Report the malaria status.
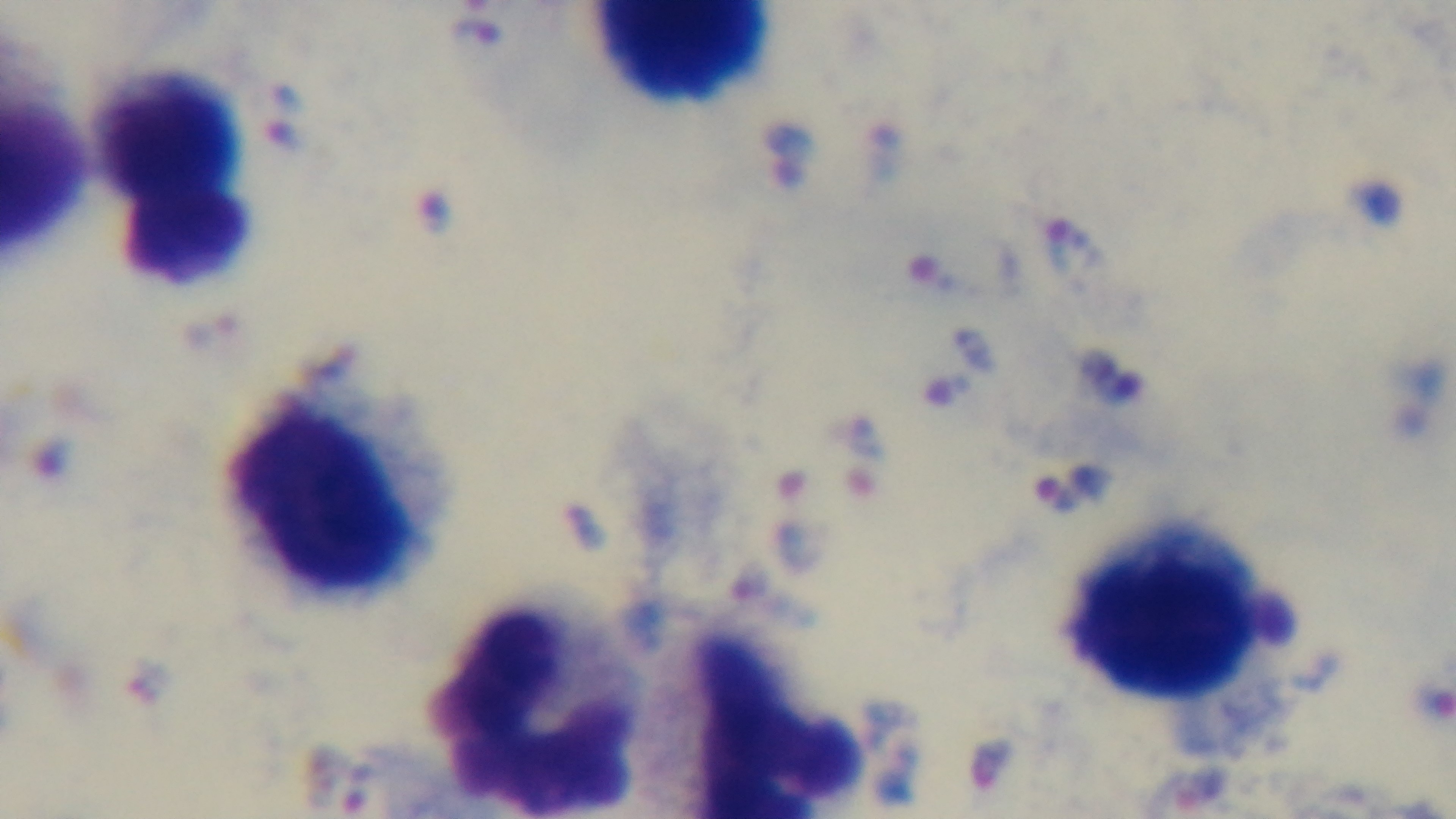

Infected.

Summary:
  - Preparation: thick blood film
  - Capture: mounted 4K digital camera
  - Modality: light microscopy
  - Stain: Giemsa
  - Field of view: single
  - Objective: 100x oil immersion